Classify this cell by malaria status.
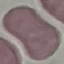

Uninfected.

{
  "preparation": "thin blood smear",
  "stain": "Giemsa",
  "capture": "smartphone through the microscope eyepiece",
  "image_type": "cell patch, automatically extracted from a larger field of view and resized to 64 × 64 pixels"
}